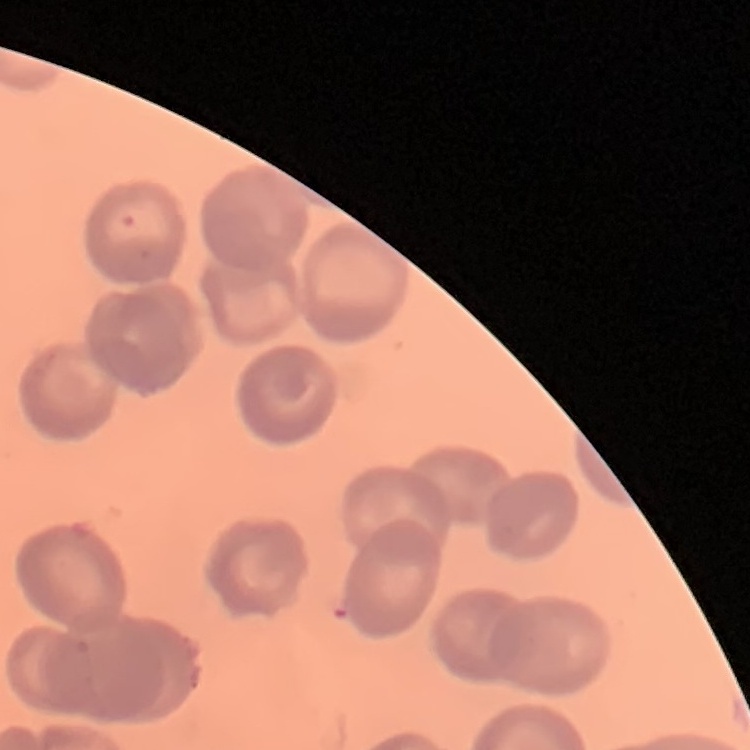

red blood cell morphology = no rouleaux formation
stain = Field's or Giemsa
preparation = thin blood film
image type = square crop of a larger photomicrograph